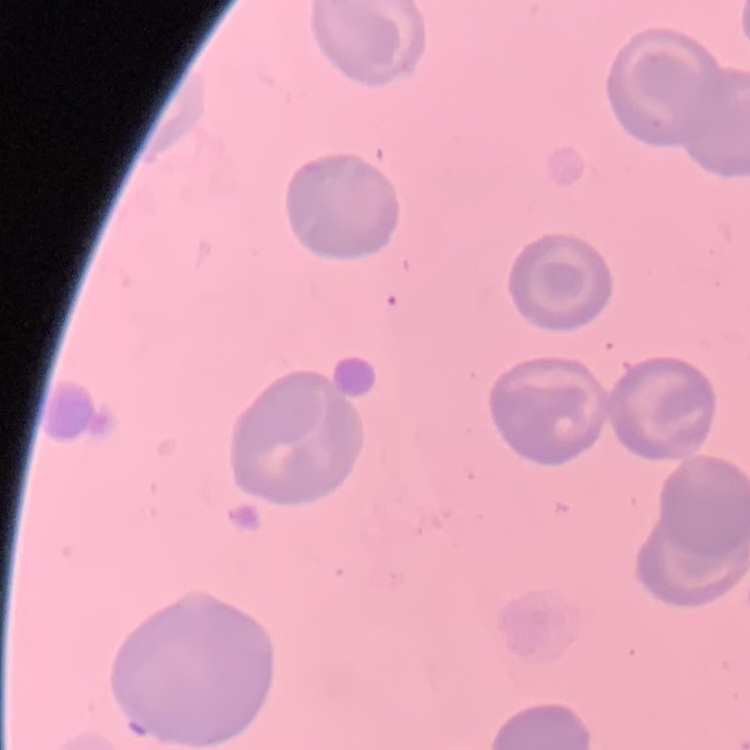

Summary:
  - Erythrocyte morphology: no rouleaux formation
  - Stain: Field's or Giemsa
  - Image type: one tile cut from a larger photomicrograph
  - Preparation: thin blood smear